Locate every blood parasite and identify its species.
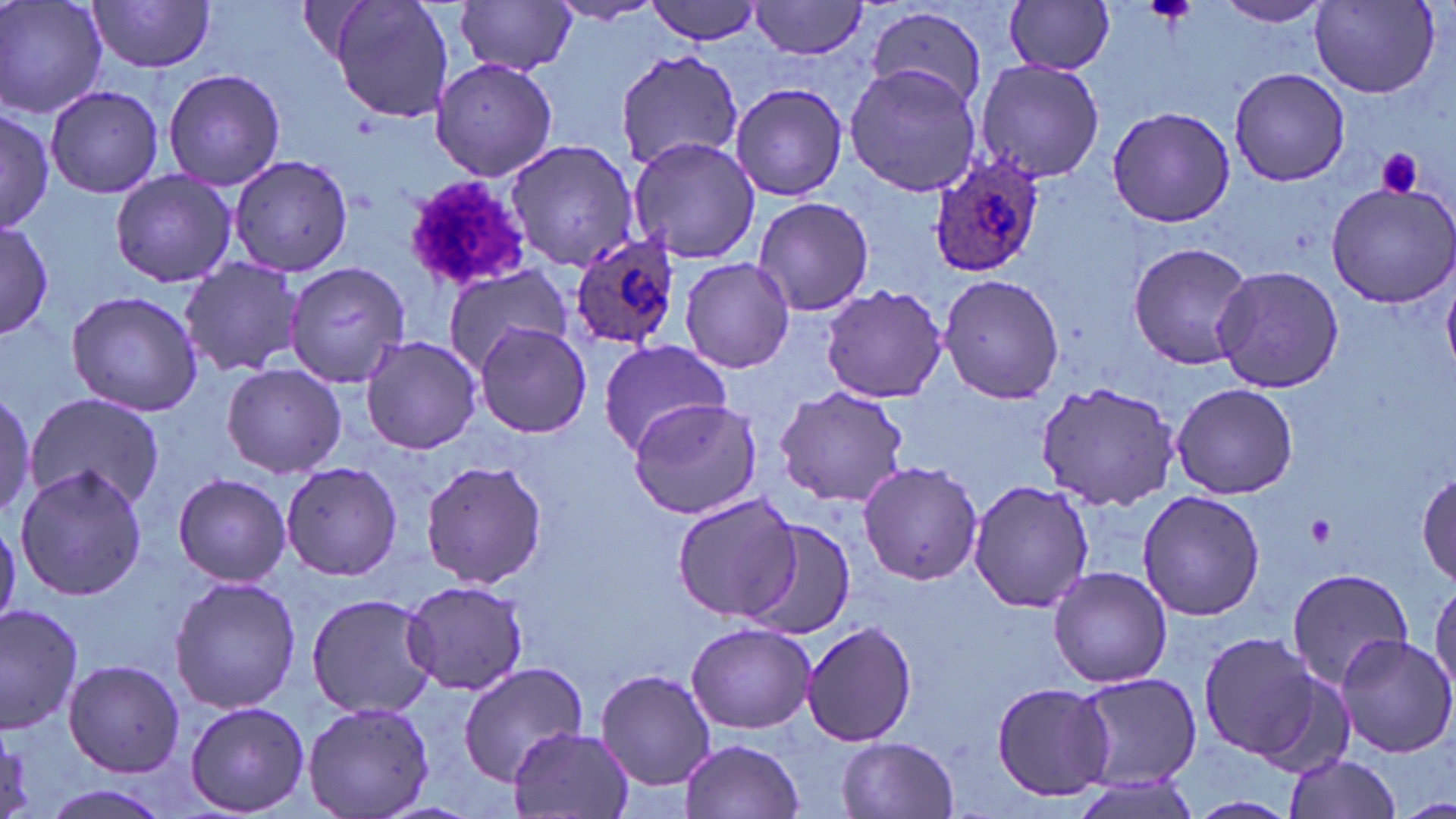
Approximate bounding boxes as [x1, y1, x2, y2] in pixels.
Plasmodium ovale-infected red blood cells: [928, 152, 1048, 280], [568, 234, 683, 355].
No Plasmodium falciparum, Plasmodium malariae, Plasmodium vivax, Babesia divergens, or Trypanosoma brucei observed.

slide-level diagnosis = Plasmodium ovale
preparation = thin blood smear
modality = light microscopy
stain = May-Grünwald-Giemsa
platelet locations = approximate bounding boxes as [x1, y1, x2, y2] in pixels: [1375, 147, 1425, 199], [399, 175, 535, 294], [1306, 513, 1337, 546]
field of view = one of a larger specimen
magnification = 1000x
image size = 1456×819 pixels
uninfected red blood cell locations = approximate bounding boxes as [x1, y1, x2, y2] in pixels: [2, 0, 108, 120], [330, 0, 455, 124], [644, 0, 761, 47], [1214, 0, 1330, 28], [89, 1, 220, 73], [458, 1, 579, 78], [1004, 1, 1116, 76], [1309, 1, 1440, 97], [550, 2, 663, 26], [750, 2, 871, 59], [863, 8, 987, 108], [616, 49, 740, 173], [431, 57, 557, 181], [971, 59, 1107, 185], [843, 64, 983, 197], [1228, 66, 1351, 186], [162, 67, 287, 191], [729, 82, 848, 202], [44, 85, 163, 200], [1106, 104, 1238, 227], [0, 106, 56, 233], [626, 135, 762, 265], [503, 140, 639, 270], [227, 154, 354, 278], [109, 169, 236, 287], [1324, 177, 1456, 309], [752, 195, 875, 317], [0, 213, 55, 344], [1127, 240, 1253, 371], [179, 255, 303, 378], [680, 256, 796, 374], [285, 260, 413, 389], [441, 264, 573, 376], [1210, 265, 1345, 393], [1443, 272, 1456, 377], [938, 273, 1064, 406], [819, 285, 949, 403], [65, 289, 204, 417], [475, 323, 592, 440], [360, 335, 482, 455], [597, 339, 731, 455], [221, 362, 347, 479], [1032, 377, 1180, 511], [1169, 382, 1298, 499], [771, 386, 910, 509], [0, 389, 38, 525], [25, 391, 163, 514], [626, 396, 765, 519], [419, 460, 548, 589], [857, 461, 985, 586], [281, 462, 403, 581], [14, 464, 149, 600], [1414, 470, 1455, 590], [172, 472, 293, 586], [965, 478, 1094, 614], [1138, 490, 1266, 620], [672, 491, 804, 623], [739, 518, 858, 640], [1047, 567, 1172, 687], [1286, 567, 1415, 693], [168, 574, 300, 715], [401, 579, 529, 696], [1429, 579, 1456, 702], [305, 593, 439, 719], [0, 601, 82, 734], [802, 620, 919, 747], [686, 621, 815, 735], [1195, 631, 1329, 766], [1334, 633, 1456, 758], [63, 659, 185, 777], [458, 662, 591, 785], [593, 668, 718, 791], [1072, 671, 1203, 791], [990, 680, 1115, 804], [184, 700, 310, 816], [299, 700, 438, 819], [510, 725, 632, 819], [837, 735, 961, 819], [679, 737, 806, 819], [1283, 753, 1403, 819], [1070, 773, 1205, 819], [36, 784, 176, 819], [1182, 795, 1301, 819]